Report the malaria status of this cell.
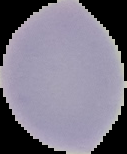

It is uninfected.

Summary:
  - Preparation: thin blood film
  - Image size: 127×154 pixels
  - Image type: segmented cell region on a black background